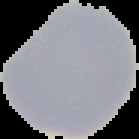
Summary:
  - Malaria status: uninfected
  - Image type: segmented cell region on a black background
  - Image size: 139×139 pixels
  - Preparation: thin blood film